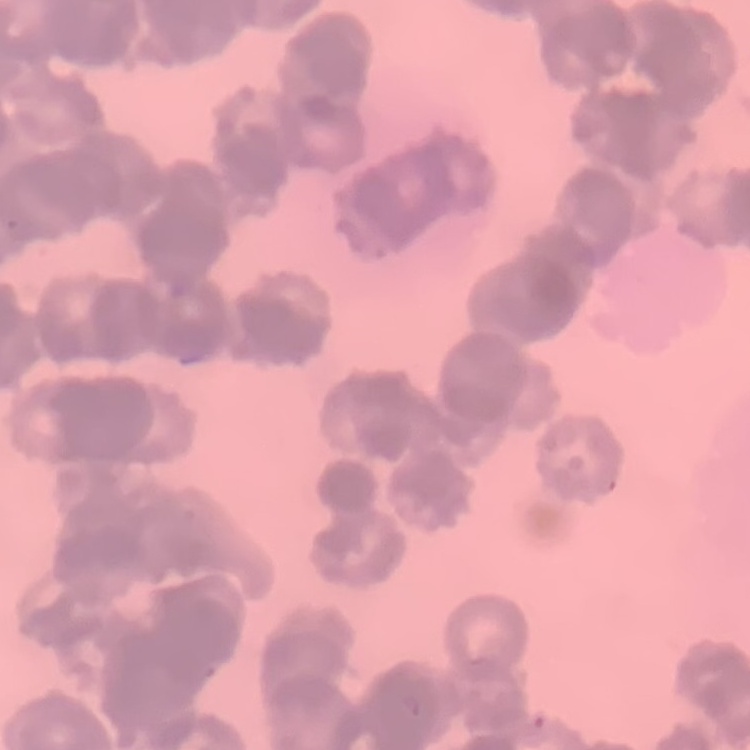
red blood cell morphology = rouleaux formation
stain = Field's or Giemsa
image type = square crop of a larger photomicrograph
preparation = thin blood smear